Classify this cell by malaria status.
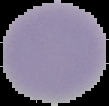
Uninfected.

Summary:
  - Image size: 109×106 pixels
  - Image type: segmented cell region with the area outside set to black
  - Preparation: thin blood smear